Report the malaria status of this cell.
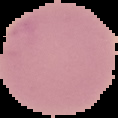

It is uninfected.

Summary:
  - Image size: 118×118 pixels
  - Image type: segmented cell region on a black background
  - Preparation: thin blood smear